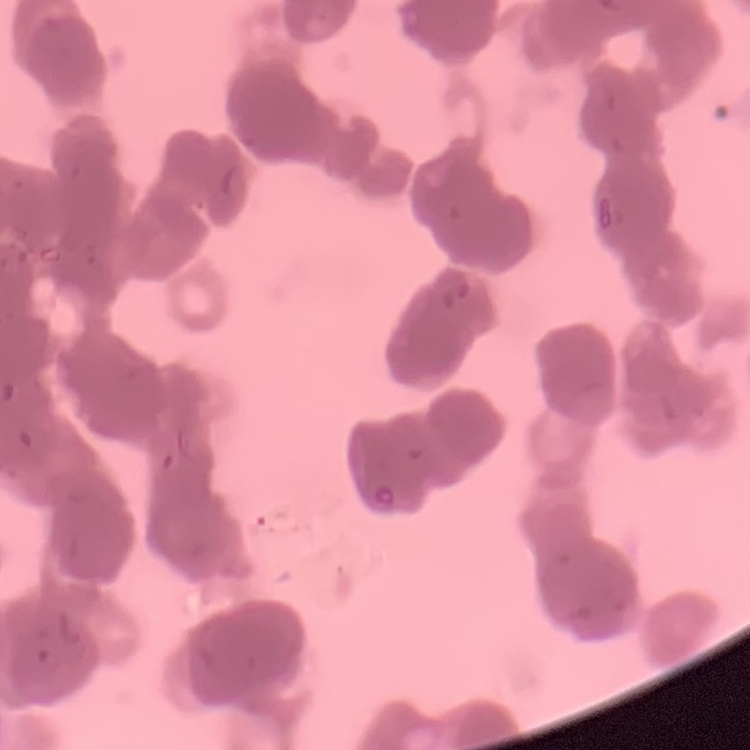
erythrocyte morphology = rouleaux formation
preparation = thin blood smear
stain = Field's or Giemsa
image type = square crop of a larger photomicrograph